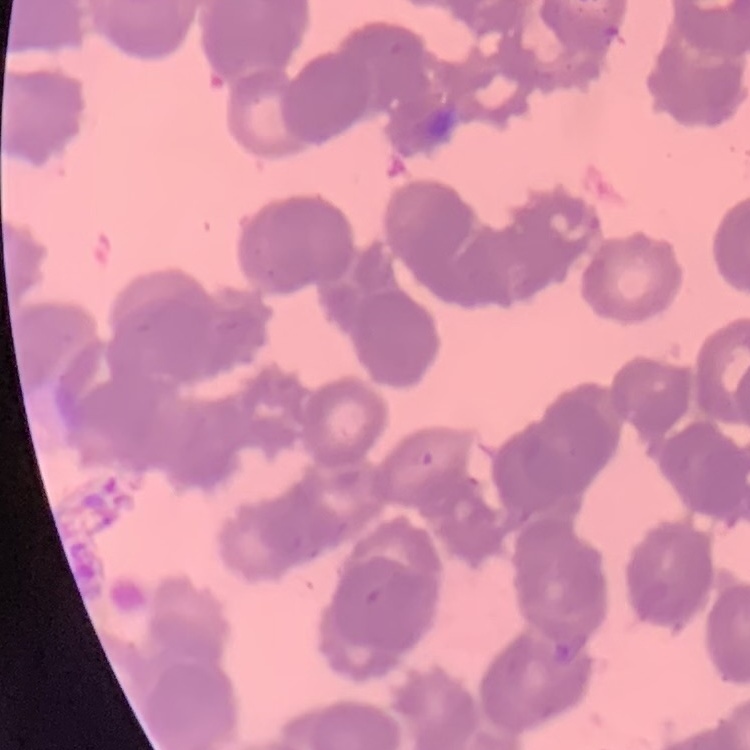

{
  "erythrocyte_morphology": "rouleaux formation",
  "stain": "Field's or Giemsa",
  "image_type": "square crop of a larger photomicrograph",
  "preparation": "thin peripheral smear"
}